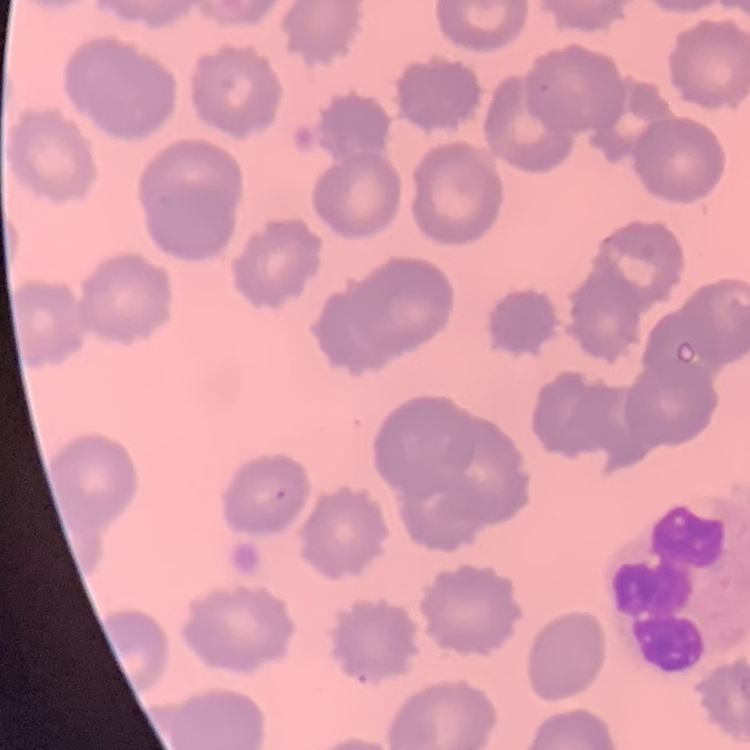
The erythrocytes show no rouleaux formation. One tile cut from a larger photomicrograph. Thin peripheral smear. Field's or Giemsa stain.